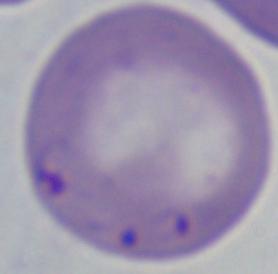 A Babesia parasite is seen. 1000x magnification. Micrograph.